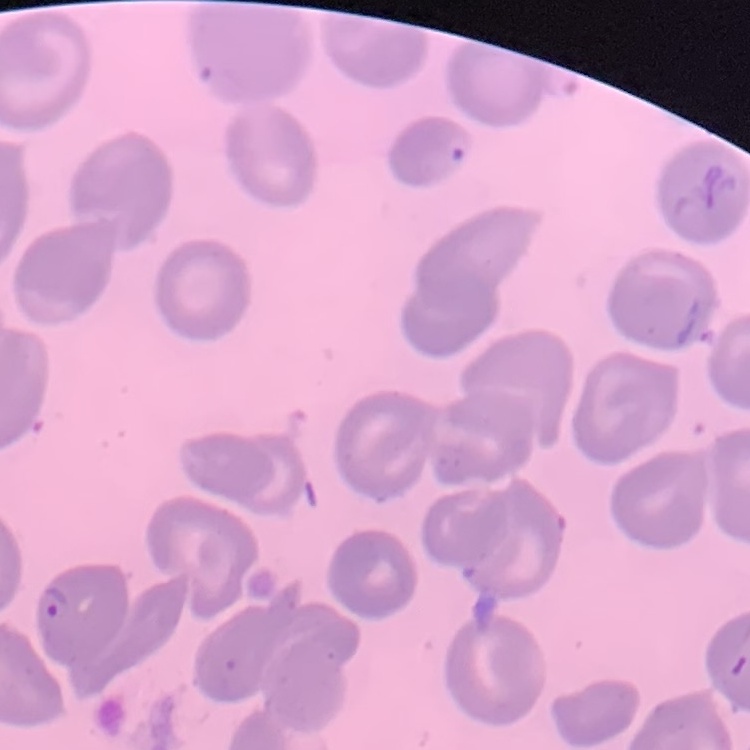 The red blood cells show no rouleaux formation. Thin peripheral smear. Square crop of a larger photomicrograph. Field's or Giemsa stain.